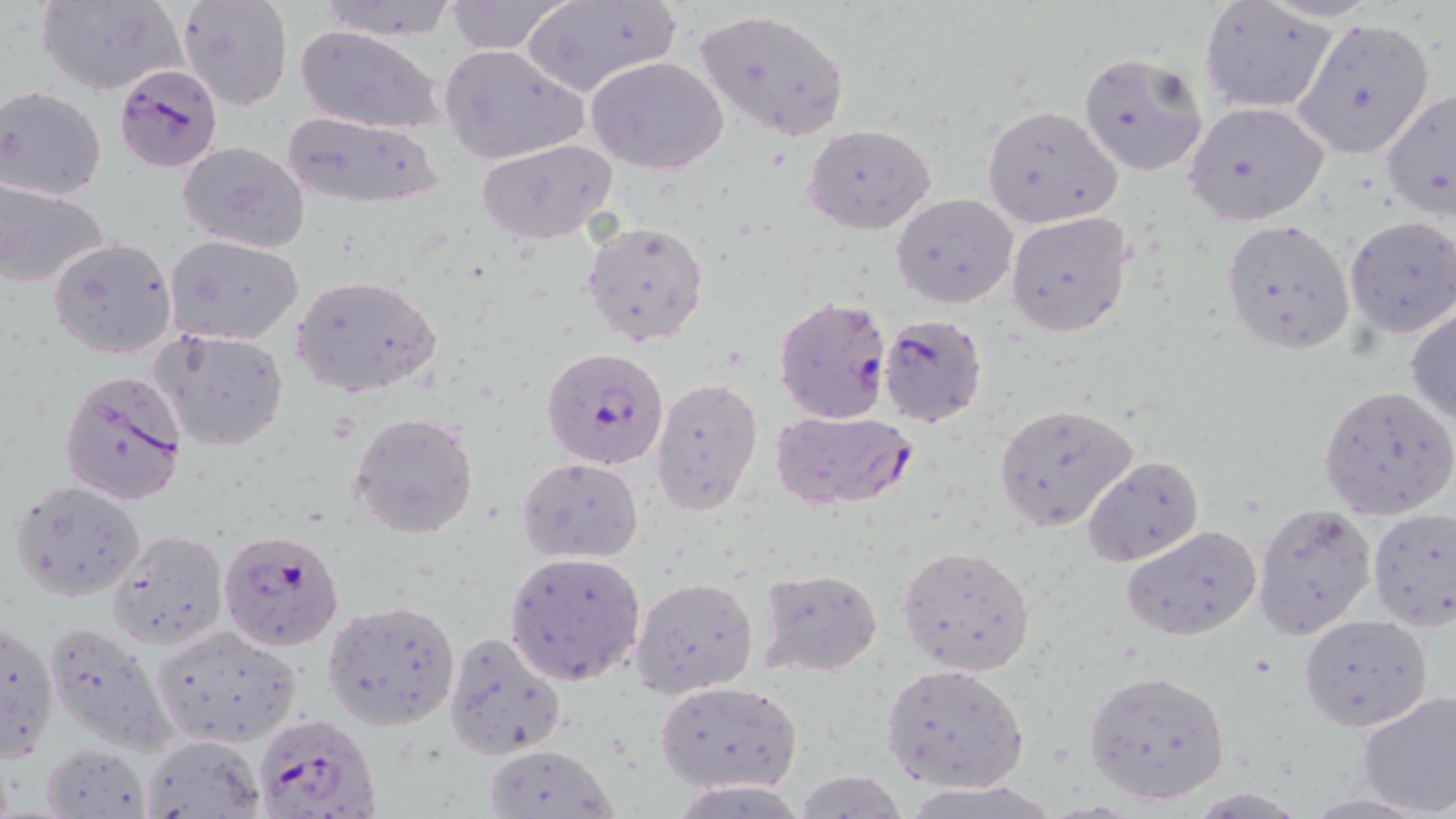

Plasmodium falciparum-infected red blood cell locations = approximate bounding boxes as named x1/y1/x2/y2 corners in pixels: (x1=118, y1=62, x2=225, y2=173), (x1=774, y1=294, x2=891, y2=426), (x1=878, y1=315, x2=987, y2=427), (x1=541, y1=346, x2=671, y2=469), (x1=57, y1=369, x2=190, y2=504), (x1=769, y1=407, x2=917, y2=510), (x1=218, y1=529, x2=345, y2=651), (x1=251, y1=712, x2=380, y2=819)
slide-level diagnosis = Plasmodium falciparum
modality = light microscopy
magnification = 1000x
stain = May-Grünwald-Giemsa
uninfected red blood cell locations = approximate bounding boxes as named x1/y1/x2/y2 corners in pixels: (x1=36, y1=0, x2=187, y2=96), (x1=310, y1=0, x2=464, y2=41), (x1=442, y1=1, x2=572, y2=54), (x1=521, y1=1, x2=682, y2=99), (x1=177, y1=2, x2=293, y2=111), (x1=1198, y1=2, x2=1339, y2=115), (x1=693, y1=9, x2=852, y2=142), (x1=1291, y1=17, x2=1438, y2=161), (x1=294, y1=25, x2=446, y2=135), (x1=440, y1=43, x2=587, y2=165), (x1=1077, y1=52, x2=1209, y2=177), (x1=586, y1=55, x2=729, y2=174), (x1=0, y1=86, x2=106, y2=201), (x1=1379, y1=87, x2=1455, y2=221), (x1=1182, y1=102, x2=1332, y2=226), (x1=981, y1=104, x2=1121, y2=228), (x1=278, y1=112, x2=447, y2=210), (x1=803, y1=123, x2=936, y2=236), (x1=478, y1=138, x2=618, y2=245), (x1=176, y1=140, x2=311, y2=253), (x1=0, y1=180, x2=110, y2=288), (x1=892, y1=192, x2=1018, y2=309), (x1=1007, y1=209, x2=1134, y2=340), (x1=1344, y1=216, x2=1455, y2=338), (x1=1219, y1=217, x2=1356, y2=356), (x1=582, y1=219, x2=711, y2=350), (x1=165, y1=234, x2=305, y2=346), (x1=48, y1=237, x2=178, y2=359), (x1=290, y1=273, x2=441, y2=399), (x1=1406, y1=306, x2=1456, y2=425), (x1=153, y1=329, x2=290, y2=452), (x1=651, y1=376, x2=763, y2=514), (x1=1318, y1=385, x2=1456, y2=521), (x1=993, y1=401, x2=1138, y2=533), (x1=350, y1=410, x2=479, y2=540), (x1=517, y1=455, x2=643, y2=564), (x1=1082, y1=455, x2=1203, y2=567), (x1=10, y1=480, x2=146, y2=601), (x1=1252, y1=502, x2=1378, y2=641), (x1=1366, y1=507, x2=1455, y2=628), (x1=1121, y1=524, x2=1261, y2=640), (x1=107, y1=529, x2=229, y2=649), (x1=898, y1=545, x2=1036, y2=676), (x1=503, y1=551, x2=646, y2=684), (x1=755, y1=567, x2=882, y2=676), (x1=631, y1=577, x2=758, y2=698), (x1=322, y1=598, x2=461, y2=732), (x1=1298, y1=613, x2=1433, y2=730), (x1=0, y1=619, x2=59, y2=761), (x1=41, y1=619, x2=181, y2=759), (x1=149, y1=624, x2=303, y2=748), (x1=442, y1=630, x2=568, y2=759), (x1=882, y1=662, x2=1029, y2=791), (x1=1082, y1=669, x2=1232, y2=807), (x1=654, y1=681, x2=801, y2=792), (x1=1355, y1=691, x2=1456, y2=816), (x1=140, y1=734, x2=266, y2=818), (x1=480, y1=742, x2=619, y2=819), (x1=41, y1=744, x2=149, y2=815), (x1=791, y1=772, x2=913, y2=817)
image size = 1456×819 pixels
field of view = one of a larger specimen
preparation = thin blood smear